Assess this cell for malaria.
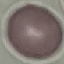
It is uninfected.

stain = Giemsa
capture = smartphone camera at the microscope eyepiece
image type = cell patch, automatically extracted from a larger field of view and resized to 64 × 64 pixels
preparation = thin blood smear